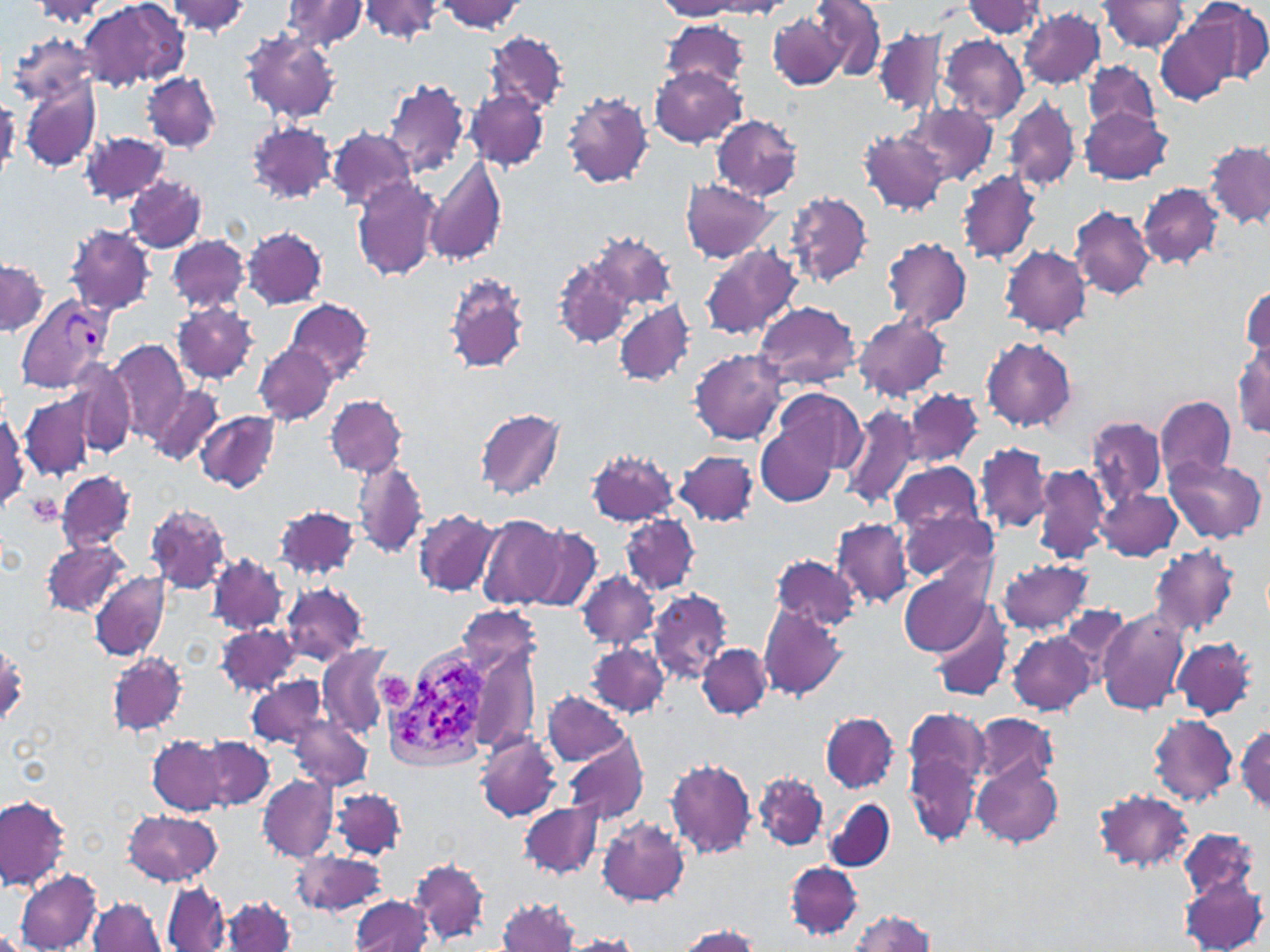
slide-level diagnosis = Plasmodium vivax
uninfected red blood cell locations = approximate bounding boxes as named x1/y1/x2/y2 corners in pixels: (x1=78, y1=0, x2=189, y2=91), (x1=164, y1=0, x2=252, y2=35), (x1=279, y1=0, x2=368, y2=54), (x1=436, y1=0, x2=524, y2=34), (x1=1186, y1=0, x2=1270, y2=85), (x1=31, y1=1, x2=110, y2=28), (x1=357, y1=1, x2=446, y2=45), (x1=657, y1=1, x2=748, y2=19), (x1=813, y1=1, x2=887, y2=81), (x1=960, y1=1, x2=1048, y2=39), (x1=1100, y1=1, x2=1190, y2=53), (x1=688, y1=2, x2=793, y2=18), (x1=1019, y1=8, x2=1106, y2=89), (x1=768, y1=11, x2=848, y2=89), (x1=1156, y1=16, x2=1243, y2=107), (x1=663, y1=21, x2=750, y2=90), (x1=874, y1=28, x2=947, y2=115), (x1=239, y1=30, x2=340, y2=124), (x1=8, y1=31, x2=99, y2=108), (x1=486, y1=31, x2=566, y2=115), (x1=939, y1=35, x2=1029, y2=122), (x1=1083, y1=59, x2=1160, y2=132), (x1=649, y1=66, x2=747, y2=148), (x1=141, y1=71, x2=221, y2=152), (x1=20, y1=77, x2=100, y2=170), (x1=383, y1=79, x2=470, y2=182), (x1=466, y1=90, x2=549, y2=170), (x1=561, y1=90, x2=653, y2=189), (x1=1004, y1=94, x2=1082, y2=195), (x1=908, y1=103, x2=996, y2=187), (x1=1080, y1=105, x2=1171, y2=185), (x1=711, y1=116, x2=802, y2=200), (x1=246, y1=120, x2=337, y2=204), (x1=327, y1=127, x2=416, y2=211), (x1=859, y1=128, x2=950, y2=216), (x1=80, y1=130, x2=170, y2=207), (x1=1205, y1=140, x2=1270, y2=230), (x1=424, y1=153, x2=508, y2=268), (x1=958, y1=169, x2=1041, y2=265), (x1=123, y1=174, x2=208, y2=254), (x1=351, y1=177, x2=442, y2=283), (x1=681, y1=179, x2=779, y2=262), (x1=1137, y1=182, x2=1224, y2=269), (x1=785, y1=192, x2=872, y2=288), (x1=1069, y1=205, x2=1156, y2=302), (x1=65, y1=224, x2=155, y2=318), (x1=242, y1=225, x2=328, y2=310), (x1=591, y1=232, x2=676, y2=312), (x1=168, y1=234, x2=248, y2=315), (x1=880, y1=238, x2=973, y2=333), (x1=700, y1=244, x2=803, y2=341), (x1=1001, y1=246, x2=1092, y2=337), (x1=1, y1=257, x2=49, y2=336), (x1=554, y1=257, x2=637, y2=349), (x1=442, y1=272, x2=530, y2=376), (x1=1241, y1=285, x2=1269, y2=369), (x1=285, y1=298, x2=374, y2=385), (x1=610, y1=300, x2=691, y2=386), (x1=754, y1=301, x2=861, y2=389), (x1=171, y1=302, x2=258, y2=384), (x1=853, y1=314, x2=951, y2=401), (x1=980, y1=336, x2=1078, y2=433), (x1=109, y1=341, x2=189, y2=442), (x1=253, y1=341, x2=338, y2=427), (x1=1234, y1=343, x2=1270, y2=438), (x1=690, y1=348, x2=786, y2=444), (x1=70, y1=359, x2=135, y2=456), (x1=148, y1=382, x2=224, y2=466), (x1=904, y1=389, x2=983, y2=467), (x1=775, y1=390, x2=867, y2=476), (x1=20, y1=394, x2=92, y2=478), (x1=325, y1=394, x2=408, y2=478), (x1=1156, y1=396, x2=1236, y2=484), (x1=754, y1=400, x2=845, y2=507), (x1=839, y1=400, x2=922, y2=511), (x1=475, y1=407, x2=566, y2=499), (x1=196, y1=409, x2=280, y2=494), (x1=1, y1=410, x2=29, y2=510), (x1=1086, y1=414, x2=1167, y2=507), (x1=976, y1=441, x2=1052, y2=534), (x1=586, y1=447, x2=681, y2=526), (x1=675, y1=449, x2=758, y2=527), (x1=1165, y1=454, x2=1267, y2=544), (x1=352, y1=459, x2=430, y2=562), (x1=890, y1=461, x2=985, y2=542), (x1=1033, y1=462, x2=1110, y2=565), (x1=56, y1=470, x2=135, y2=551), (x1=1096, y1=487, x2=1181, y2=562), (x1=145, y1=503, x2=232, y2=594), (x1=274, y1=505, x2=363, y2=582), (x1=901, y1=505, x2=998, y2=586), (x1=413, y1=508, x2=503, y2=597), (x1=620, y1=513, x2=701, y2=597), (x1=476, y1=515, x2=565, y2=610), (x1=830, y1=519, x2=911, y2=607), (x1=519, y1=525, x2=604, y2=610), (x1=40, y1=539, x2=130, y2=618), (x1=1148, y1=543, x2=1240, y2=639), (x1=770, y1=553, x2=865, y2=635), (x1=209, y1=554, x2=287, y2=635), (x1=996, y1=558, x2=1093, y2=635), (x1=898, y1=566, x2=994, y2=658), (x1=89, y1=570, x2=170, y2=660), (x1=577, y1=571, x2=659, y2=649), (x1=280, y1=581, x2=369, y2=665), (x1=647, y1=587, x2=733, y2=684), (x1=758, y1=602, x2=847, y2=702), (x1=932, y1=604, x2=1012, y2=702), (x1=1055, y1=606, x2=1132, y2=681), (x1=1094, y1=606, x2=1188, y2=714), (x1=215, y1=622, x2=301, y2=696), (x1=1007, y1=631, x2=1097, y2=715), (x1=1170, y1=637, x2=1258, y2=720), (x1=0, y1=641, x2=26, y2=726), (x1=464, y1=641, x2=542, y2=757), (x1=588, y1=642, x2=669, y2=718), (x1=318, y1=643, x2=395, y2=738), (x1=697, y1=644, x2=771, y2=719), (x1=107, y1=652, x2=187, y2=736), (x1=248, y1=677, x2=328, y2=750), (x1=542, y1=691, x2=633, y2=765), (x1=901, y1=705, x2=989, y2=846), (x1=973, y1=712, x2=1059, y2=787), (x1=821, y1=713, x2=899, y2=792), (x1=1149, y1=714, x2=1238, y2=805), (x1=291, y1=715, x2=371, y2=788), (x1=1234, y1=724, x2=1269, y2=816), (x1=476, y1=732, x2=561, y2=822), (x1=147, y1=734, x2=229, y2=815), (x1=196, y1=735, x2=276, y2=810), (x1=563, y1=737, x2=648, y2=825), (x1=664, y1=757, x2=756, y2=859), (x1=973, y1=758, x2=1063, y2=849), (x1=755, y1=771, x2=828, y2=850), (x1=257, y1=774, x2=338, y2=862), (x1=332, y1=787, x2=406, y2=861), (x1=1091, y1=789, x2=1196, y2=874), (x1=0, y1=795, x2=70, y2=890), (x1=825, y1=799, x2=895, y2=872), (x1=518, y1=801, x2=602, y2=879), (x1=122, y1=809, x2=222, y2=885), (x1=596, y1=816, x2=690, y2=907), (x1=1179, y1=828, x2=1262, y2=903), (x1=292, y1=848, x2=387, y2=917), (x1=410, y1=858, x2=488, y2=944), (x1=785, y1=861, x2=863, y2=940), (x1=15, y1=871, x2=100, y2=950), (x1=1177, y1=873, x2=1266, y2=952), (x1=162, y1=881, x2=230, y2=952), (x1=220, y1=894, x2=296, y2=952), (x1=351, y1=896, x2=431, y2=950), (x1=497, y1=896, x2=577, y2=951), (x1=87, y1=897, x2=165, y2=952), (x1=847, y1=910, x2=939, y2=952), (x1=673, y1=925, x2=761, y2=951), (x1=559, y1=934, x2=642, y2=951)
magnification = 1000x
platelet locations = approximate bounding boxes as named x1/y1/x2/y2 corners in pixels: (x1=24, y1=494, x2=63, y2=525)
stain = May-Grünwald-Giemsa
Plasmodium vivax-infected red blood cell locations = approximate bounding boxes as named x1/y1/x2/y2 corners in pixels: (x1=18, y1=297, x2=112, y2=391), (x1=383, y1=644, x2=501, y2=773)
image size = 1270×952 pixels
field of view = one of a larger specimen
preparation = thin blood smear
modality = optical microscopy